Classify this cell by malaria status.
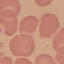

Uninfected.

preparation: thin blood smear
image_type: cell patch, automatically extracted from a larger field of view and resized to 64 × 64 pixels
capture: smartphone camera at the microscope eyepiece
stain: Giemsa